Locate every leukocyte (white blood cell).
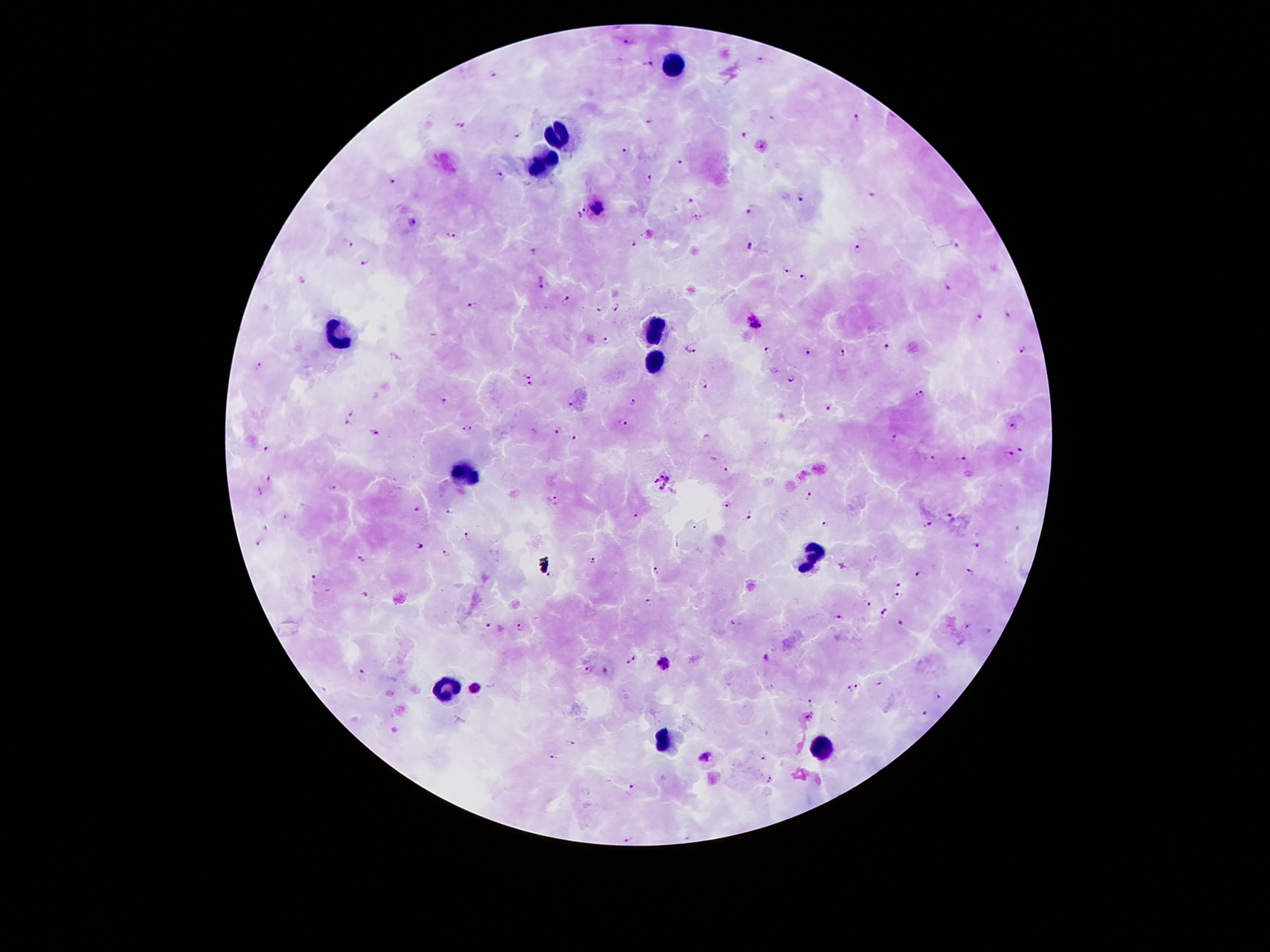
Approximate centers as (x, y) in pixels.
Leukocytes: (675, 61), (563, 133), (543, 159), (653, 324), (336, 335), (658, 357), (465, 475), (810, 556), (445, 688), (667, 741), (824, 749).

Malaria parasite locations: (628, 42), (761, 57), (648, 63), (493, 73), (772, 118), (858, 118), (650, 121), (459, 123), (746, 135), (520, 136), (764, 147), (626, 149), (680, 161), (499, 175), (649, 178), (391, 181), (801, 197), (872, 197), (690, 200), (584, 207), (597, 207), (750, 212), (580, 215), (696, 217), (411, 221), (451, 232), (350, 244), (635, 244), (956, 244), (749, 246), (856, 249), (533, 252), (364, 266), (784, 269), (803, 276), (302, 280), (541, 283), (949, 289), (567, 300), (473, 305), (599, 306), (614, 310), (1006, 317), (979, 319), (755, 325), (602, 340), (888, 345), (693, 346), (767, 348), (1023, 350), (808, 352), (842, 353), (259, 366), (527, 375), (792, 376), (704, 383), (531, 385), (919, 396), (445, 400), (633, 400), (830, 405), (352, 411), (622, 421), (346, 423), (1013, 426), (469, 427), (557, 429), (374, 435), (894, 436), (707, 437), (573, 439), (1020, 449), (270, 450), (1010, 456), (930, 457), (965, 458), (726, 469), (269, 478), (664, 482), (332, 487), (260, 492), (808, 496), (555, 500), (725, 503), (417, 508), (451, 511), (637, 516), (750, 516), (950, 516), (282, 517), (928, 523), (825, 525), (264, 529), (467, 537), (259, 542), (977, 544), (417, 545), (446, 554), (361, 559), (593, 561), (843, 567), (970, 568), (659, 571), (920, 572), (549, 576), (314, 579), (899, 583), (365, 595), (896, 595), (648, 601), (866, 603), (885, 610), (841, 617), (735, 621), (902, 621), (486, 625), (967, 625), (520, 627), (987, 630), (637, 654), (768, 656), (627, 662), (666, 665), (589, 669), (362, 671), (879, 684), (858, 685), (474, 689), (849, 689), (936, 694), (811, 701), (927, 714), (571, 742), (705, 756), (553, 757), (763, 757), (770, 778), (630, 785), (630, 837). Giemsa-stained preparation. Thick peripheral-blood smear. Patient malaria status: infected with Plasmodium falciparum. Image is 1270×952 pixels. One field from this slide. 100x magnification. Smartphone photograph taken through the microscope eyepiece.